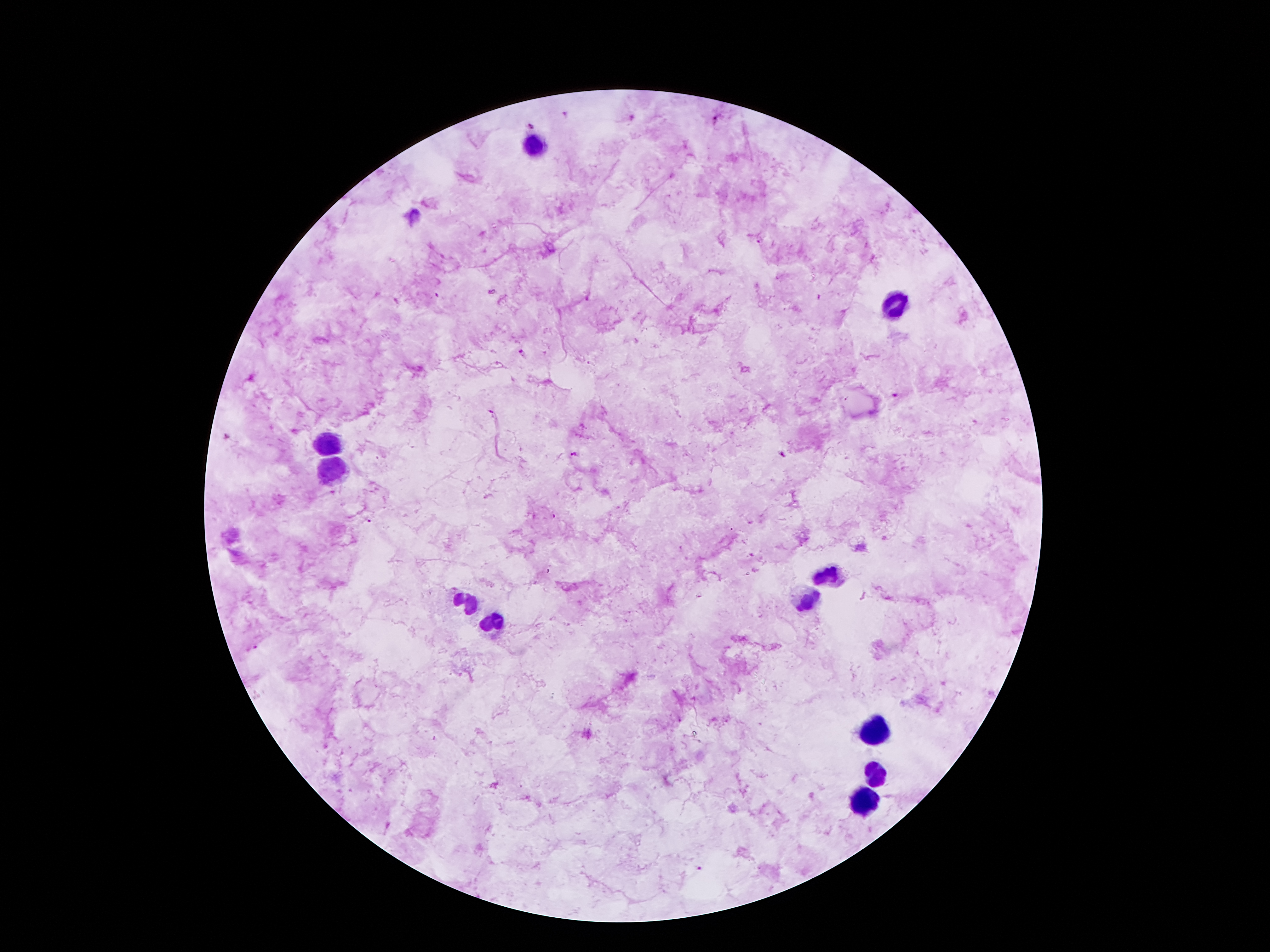 Approximate centers as (x, y) in pixels. Malaria parasite locations: (565, 117), (633, 120), (715, 120), (533, 125), (521, 353), (894, 394), (782, 455), (698, 869). Leukocyte locations: (534, 147), (894, 306), (328, 441), (332, 468), (828, 574), (463, 601), (806, 603), (492, 623), (872, 729), (874, 777), (863, 804). 100x magnification. Thick blood smear. Giemsa stain. Smartphone photograph taken through the microscope eyepiece. One field from this slide. Image is 1270×952 pixels. Patient malaria status: infected with Plasmodium falciparum.